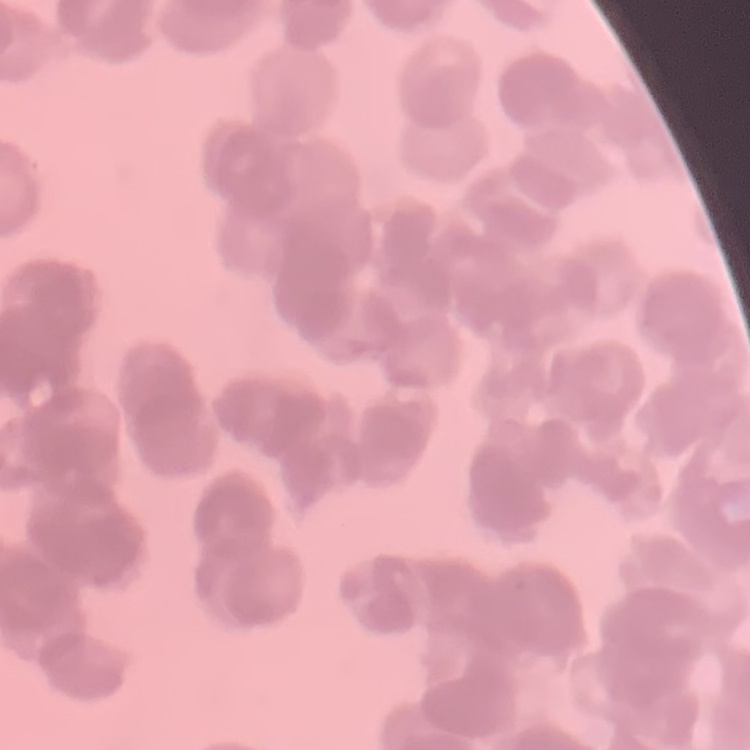
The erythrocytes exhibit rouleaux formation. Thin blood film. One tile cut from a larger photomicrograph. Stained with either Field's or Giemsa.